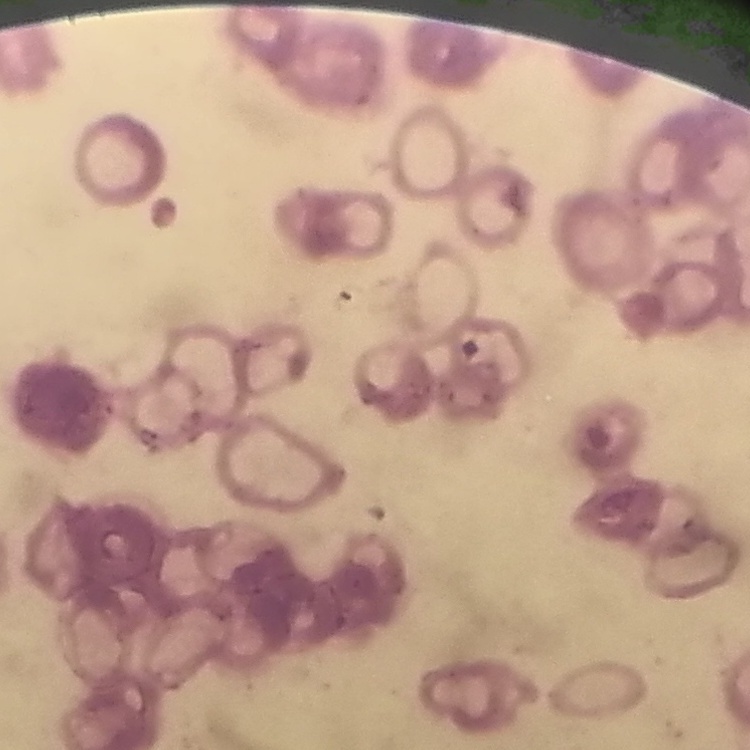
{
  "erythrocyte_morphology": "rouleaux formation",
  "preparation": "thin blood film",
  "image_type": "square crop of a larger photomicrograph",
  "stain": "Field's or Giemsa"
}